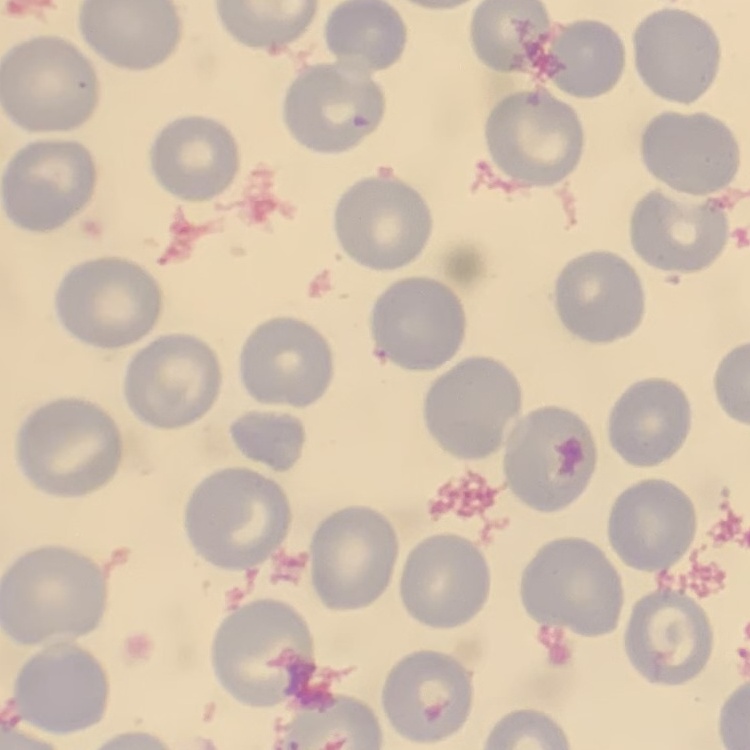 The red blood cells exhibit no rouleaux formation. Square crop of a larger photomicrograph. Field's or Giemsa stain. Thin peripheral smear.